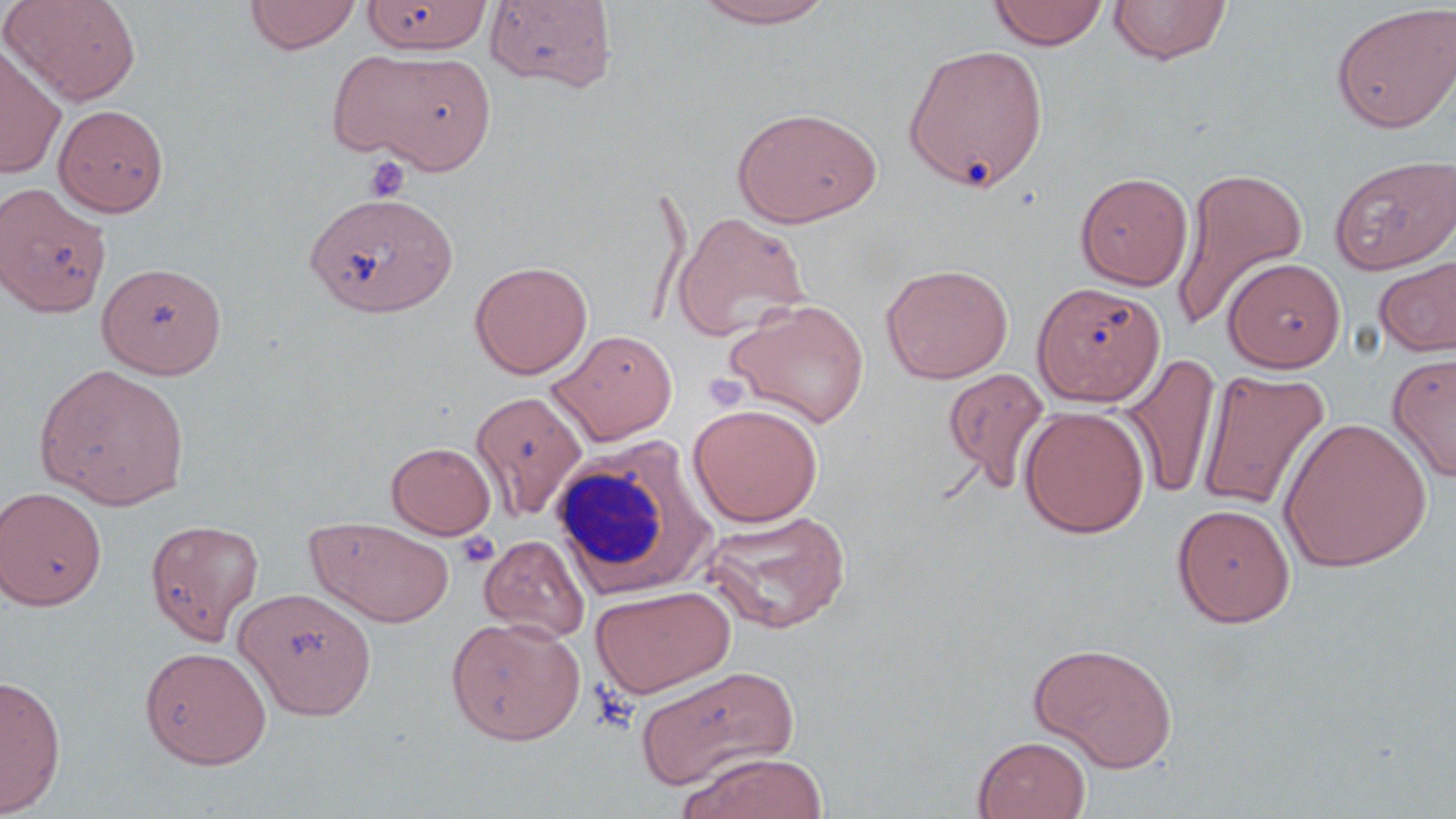
Summary:
  - Coordinate format: approximate bounding boxes as named x1/y1/x2/y2 corners in pixels
  - White blood cell locations: (x1=549, y1=435, x2=717, y2=599)
  - Uninfected red blood cell locations: (x1=1, y1=0, x2=140, y2=105), (x1=244, y1=0, x2=361, y2=54), (x1=690, y1=0, x2=840, y2=28), (x1=987, y1=0, x2=1110, y2=50), (x1=1108, y1=0, x2=1232, y2=65), (x1=361, y1=1, x2=490, y2=54), (x1=484, y1=1, x2=617, y2=92), (x1=1330, y1=4, x2=1456, y2=133), (x1=0, y1=42, x2=67, y2=180), (x1=904, y1=43, x2=1049, y2=192), (x1=338, y1=47, x2=498, y2=173), (x1=53, y1=104, x2=170, y2=217), (x1=730, y1=106, x2=882, y2=228), (x1=1330, y1=154, x2=1456, y2=274), (x1=1171, y1=166, x2=1308, y2=329), (x1=1075, y1=172, x2=1193, y2=290), (x1=0, y1=183, x2=111, y2=319), (x1=304, y1=190, x2=457, y2=318), (x1=672, y1=211, x2=811, y2=342), (x1=1373, y1=254, x2=1456, y2=357), (x1=1223, y1=257, x2=1345, y2=372), (x1=469, y1=260, x2=593, y2=379), (x1=98, y1=261, x2=226, y2=379), (x1=881, y1=263, x2=1013, y2=384), (x1=1032, y1=281, x2=1165, y2=406), (x1=725, y1=297, x2=870, y2=428), (x1=547, y1=329, x2=678, y2=445), (x1=1387, y1=352, x2=1456, y2=482), (x1=1119, y1=354, x2=1222, y2=500), (x1=34, y1=364, x2=190, y2=509), (x1=942, y1=367, x2=1050, y2=493), (x1=1196, y1=369, x2=1331, y2=512), (x1=471, y1=390, x2=589, y2=520), (x1=687, y1=403, x2=823, y2=527), (x1=1018, y1=406, x2=1151, y2=538), (x1=1277, y1=416, x2=1432, y2=573), (x1=386, y1=442, x2=496, y2=539), (x1=0, y1=486, x2=107, y2=610), (x1=1171, y1=502, x2=1296, y2=628), (x1=702, y1=509, x2=852, y2=634), (x1=305, y1=516, x2=455, y2=628), (x1=145, y1=518, x2=264, y2=644), (x1=478, y1=534, x2=590, y2=642), (x1=591, y1=585, x2=736, y2=698), (x1=233, y1=587, x2=376, y2=720), (x1=446, y1=616, x2=586, y2=745), (x1=1028, y1=642, x2=1178, y2=772), (x1=139, y1=645, x2=272, y2=769), (x1=634, y1=665, x2=800, y2=792), (x1=0, y1=673, x2=67, y2=817), (x1=973, y1=735, x2=1091, y2=819), (x1=677, y1=752, x2=829, y2=819)
  - Platelet locations: (x1=364, y1=156, x2=408, y2=202), (x1=703, y1=372, x2=748, y2=412), (x1=457, y1=532, x2=500, y2=569)
  - Slide-level diagnosis: no evidence of blood parasites
  - Image size: 1456×819 pixels
  - Preparation: thin blood smear
  - Modality: optical microscopy
  - Stain: May-Grünwald-Giemsa
  - Magnification: 1000x
  - Field of view: one of a larger specimen